Locate every blood parasite and identify its species.
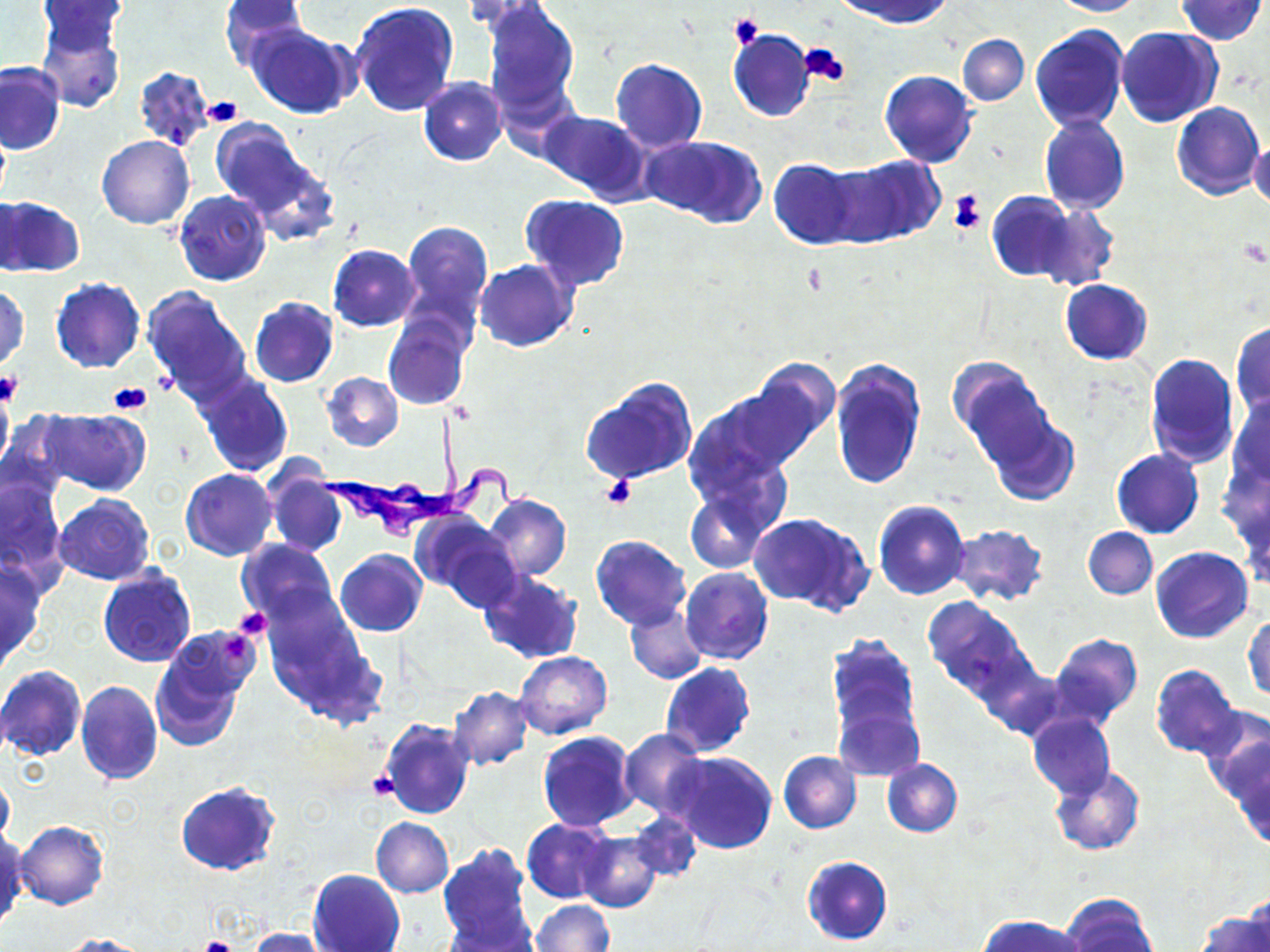
Approximate bounding boxes as [x1, y1, x2, y2] in pixels.
Trypanosoma brucei: [320, 415, 542, 542].
No Plasmodium falciparum, Plasmodium ovale, Plasmodium malariae, Plasmodium vivax, or Babesia divergens observed.

Summary:
  - Uninfected red blood cell locations: [218, 0, 309, 73], [456, 0, 548, 29], [483, 0, 580, 116], [1052, 0, 1145, 17], [1174, 0, 1268, 45], [36, 1, 131, 52], [838, 1, 958, 27], [352, 2, 458, 115], [37, 17, 124, 113], [248, 25, 355, 118], [1030, 25, 1129, 131], [1117, 26, 1222, 127], [727, 29, 814, 122], [958, 34, 1028, 105], [610, 58, 707, 152], [0, 62, 65, 154], [136, 67, 214, 149], [879, 70, 978, 168], [419, 77, 507, 166], [1172, 101, 1265, 201], [537, 109, 651, 202], [1039, 115, 1129, 214], [216, 119, 316, 222], [1249, 132, 1269, 212], [97, 135, 194, 230], [644, 136, 767, 228], [824, 154, 940, 245], [768, 158, 864, 248], [174, 190, 271, 285], [986, 190, 1076, 281], [1, 193, 26, 276], [521, 195, 629, 291], [2, 196, 83, 279], [1031, 205, 1119, 292], [401, 219, 493, 327], [328, 245, 421, 331], [475, 259, 578, 352], [51, 278, 145, 373], [1060, 279, 1153, 364], [0, 285, 29, 371], [142, 285, 252, 398], [249, 298, 338, 387], [384, 318, 471, 410], [1231, 321, 1270, 417], [1145, 354, 1240, 468], [830, 359, 926, 491], [949, 360, 1060, 470], [323, 372, 403, 450], [199, 374, 293, 476], [581, 375, 698, 486], [0, 377, 13, 482], [685, 382, 823, 501], [1228, 395, 1270, 492], [36, 408, 151, 494], [3, 410, 79, 502], [987, 415, 1079, 505], [1112, 448, 1204, 538], [264, 467, 346, 557], [179, 468, 276, 560], [0, 474, 66, 581], [686, 491, 770, 573], [484, 494, 571, 580], [53, 495, 155, 585], [874, 501, 970, 599], [750, 511, 873, 614], [412, 513, 519, 608], [950, 525, 1050, 607], [1083, 527, 1157, 599], [591, 534, 691, 629], [236, 538, 338, 627], [1152, 547, 1252, 644], [335, 550, 427, 637], [0, 562, 44, 671], [98, 566, 195, 668], [680, 567, 773, 664], [478, 570, 584, 663], [922, 595, 1037, 708], [266, 603, 379, 724], [625, 603, 707, 684], [1245, 614, 1270, 701], [161, 623, 260, 708], [1050, 633, 1142, 726], [826, 634, 922, 756], [149, 641, 249, 754], [516, 650, 611, 739], [660, 662, 756, 757], [1151, 665, 1243, 760], [0, 666, 86, 761], [76, 682, 162, 786], [449, 687, 533, 770], [831, 699, 923, 783], [1199, 706, 1270, 808], [1028, 714, 1116, 800], [380, 719, 474, 818], [618, 728, 708, 819], [538, 732, 638, 831], [1228, 746, 1270, 849], [778, 751, 861, 833], [666, 752, 777, 854], [882, 759, 962, 837], [1049, 766, 1145, 856], [0, 771, 14, 848], [176, 782, 280, 876], [629, 810, 702, 882], [370, 816, 454, 897], [521, 817, 615, 903], [15, 821, 107, 909], [1, 830, 27, 927], [577, 831, 662, 912], [438, 843, 532, 949], [802, 856, 892, 945], [309, 868, 404, 951], [1063, 894, 1158, 952], [1243, 895, 1270, 951], [532, 900, 615, 952], [1200, 910, 1269, 952], [439, 912, 536, 952], [980, 914, 1089, 951], [250, 927, 334, 952], [59, 933, 153, 952]
  - Platelet locations: [729, 12, 762, 49], [798, 41, 851, 89], [204, 97, 242, 129], [949, 188, 985, 234], [0, 369, 23, 406], [108, 381, 153, 417], [602, 474, 638, 508], [232, 608, 271, 641], [224, 635, 246, 661], [367, 771, 398, 798], [192, 938, 243, 952]
  - Slide-level diagnosis: Trypanosoma brucei
  - Stain: May-Grünwald-Giemsa
  - Preparation: thin blood smear
  - Image size: 1270×952 pixels
  - Field of view: one of a larger specimen
  - Modality: optical microscopy
  - Magnification: 1000x